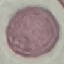 Result: no malaria parasites detected. Automatically extracted cell patch, resized to 64 × 64 pixels. Giemsa stain. Thin blood film. Acquired by smartphone through the microscope eyepiece.